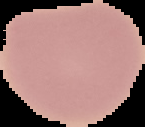

malaria status = uninfected
preparation = thin blood smear
image type = cell region segmented out of the field of view; surrounding area masked to black
image size = 145×127 pixels